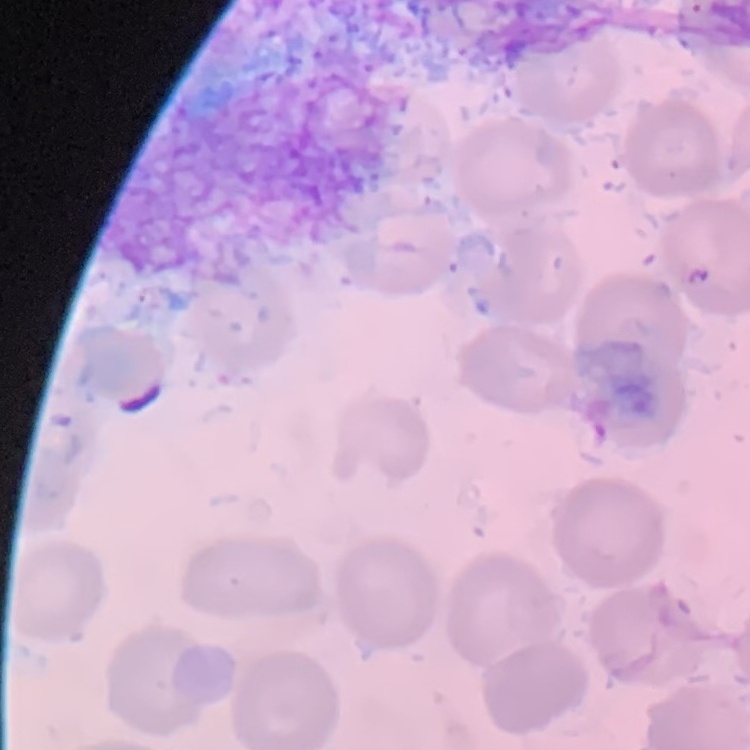
{
  "red_blood_cell_morphology": "no rouleaux formation",
  "stain": "Field's or Giemsa",
  "preparation": "thin blood smear",
  "image_type": "one tile cut from a larger photomicrograph"
}